Name the parasite shown.
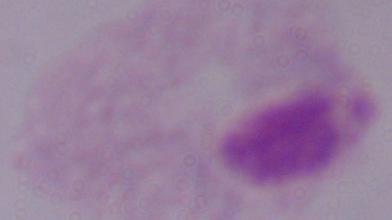
A trichomonad.

Photomicrograph. Captured at 1000x magnification.